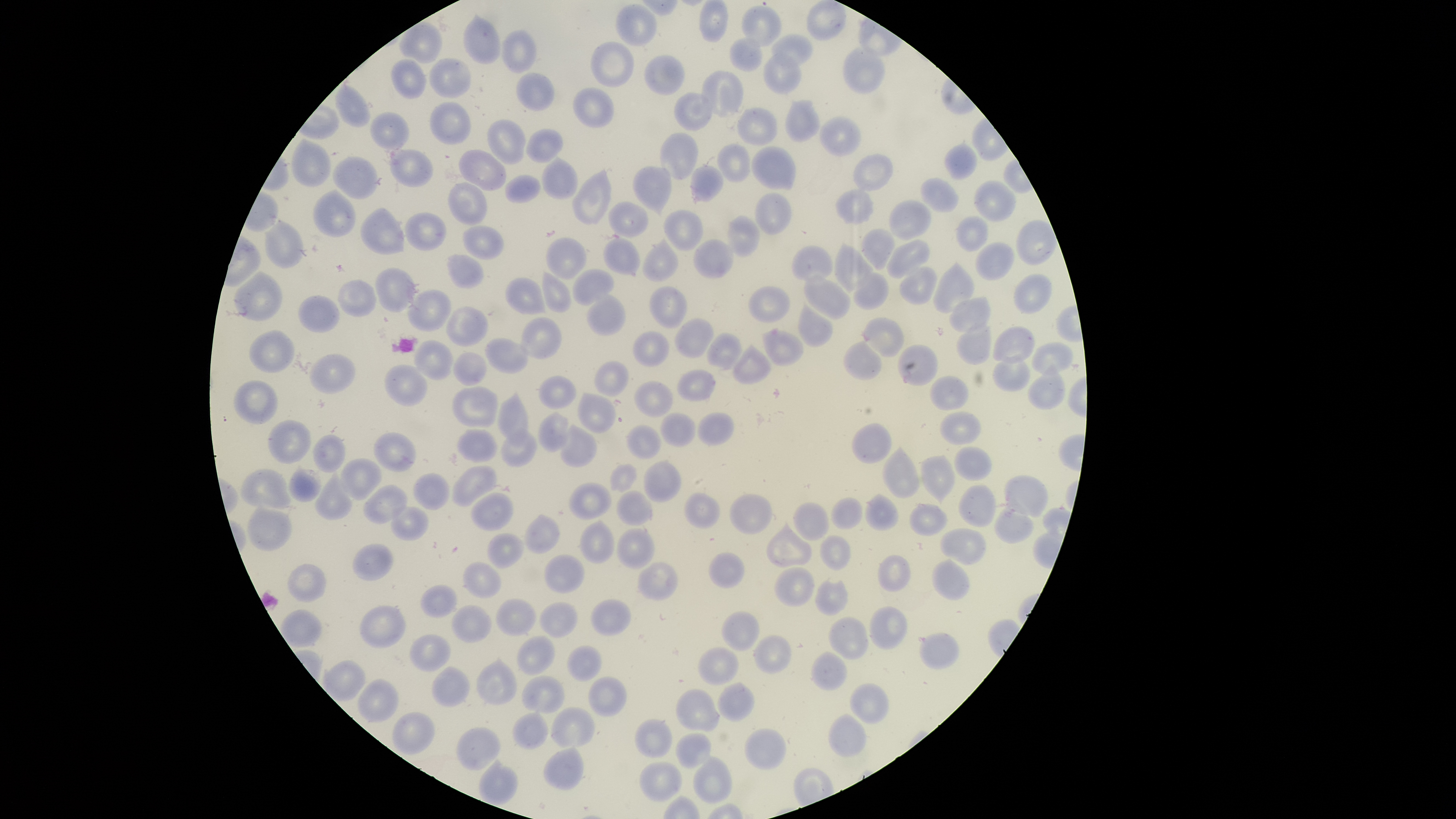
image_size: 1456×819 pixels
presence: no malaria parasites identified
capture: smartphone photograph through the microscope eyepiece
field_of_view: single
preparation: thin blood film
uninfected_red_blood_cells: 'approximate bounding boxes as (left, top, right, bottom) in pixels: (699, 0, 729, 43), (805, 1, 847, 40), (615, 3, 658, 46), (742, 6, 782, 47), (463, 12, 501, 64), (399, 22, 442, 63), (500, 29, 537, 73), (772, 33, 813, 67), (729, 37, 761, 71), (590, 41, 635, 87), (842, 47, 886, 94), (763, 53, 801, 95), (644, 55, 685, 96), (391, 58, 427, 99), (429, 59, 471, 99), (515, 71, 555, 112), (702, 71, 743, 116), (333, 85, 370, 127), (572, 87, 614, 128), (674, 92, 712, 131), (784, 99, 821, 144), (430, 101, 472, 144), (737, 106, 778, 146), (370, 112, 409, 148), (819, 116, 861, 157), (487, 119, 527, 164), (524, 127, 564, 163), (660, 133, 698, 179), (292, 138, 330, 188), (944, 142, 978, 181), (716, 144, 751, 184), (752, 146, 796, 191), (390, 149, 432, 187), (457, 149, 506, 192), (853, 153, 893, 192), (542, 155, 578, 199), (332, 156, 378, 199), (690, 164, 724, 203), (633, 166, 672, 217), (573, 168, 611, 226), (504, 174, 540, 203), (920, 177, 958, 212), (973, 181, 1016, 223), (449, 182, 489, 226), (835, 188, 875, 225), (313, 189, 356, 237), (756, 192, 792, 236), (888, 199, 932, 242), (609, 201, 647, 237), (360, 207, 405, 255), (663, 210, 702, 250), (405, 212, 447, 250), (727, 214, 759, 257), (957, 215, 989, 252), (263, 218, 304, 268), (1015, 220, 1057, 265), (461, 225, 504, 259), (860, 227, 896, 271), (545, 237, 587, 279), (643, 237, 679, 282), (603, 238, 640, 275), (693, 239, 733, 279), (886, 239, 930, 279), (835, 241, 873, 293), (974, 242, 1014, 281), (792, 246, 832, 282), (446, 254, 483, 289), (933, 262, 974, 314), (899, 265, 937, 305), (375, 267, 419, 312), (572, 269, 614, 306), (235, 270, 283, 321), (542, 271, 572, 313), (804, 271, 852, 319), (853, 272, 887, 310), (1013, 274, 1051, 314), (506, 277, 546, 315), (338, 279, 375, 316), (649, 285, 687, 329), (748, 285, 790, 322), (406, 289, 453, 332), (587, 294, 626, 336), (298, 295, 338, 333), (949, 296, 990, 333), (797, 302, 833, 348), (445, 306, 488, 346), (519, 317, 562, 359), (673, 317, 713, 358), (863, 317, 904, 358), (957, 321, 989, 363), (993, 325, 1034, 365), (762, 329, 804, 367), (249, 330, 296, 372), (633, 331, 670, 367), (706, 332, 743, 372), (485, 338, 530, 373), (842, 339, 882, 380), (413, 340, 454, 381), (732, 342, 771, 384), (1032, 343, 1073, 375), (896, 344, 939, 385), (452, 352, 487, 386), (310, 353, 355, 394), (992, 357, 1031, 391), (593, 361, 628, 397), (1028, 363, 1064, 410), (384, 364, 428, 407), (676, 369, 715, 401), (537, 376, 577, 409), (930, 376, 969, 409), (234, 380, 277, 425), (634, 380, 673, 417), (453, 387, 498, 427), (498, 391, 528, 448), (577, 392, 616, 434), (539, 411, 568, 452), (659, 412, 697, 448), (697, 412, 734, 446), (940, 412, 982, 444), (268, 420, 311, 463), (561, 423, 598, 468), (851, 423, 891, 464), (625, 425, 661, 459), (501, 427, 537, 466), (456, 428, 498, 462), (373, 432, 417, 472), (311, 434, 345, 472), (882, 445, 920, 499), (953, 446, 992, 481), (921, 454, 956, 506), (340, 459, 381, 500), (643, 460, 681, 502), (610, 463, 637, 493), (287, 464, 321, 502), (451, 466, 497, 507), (241, 469, 291, 509), (315, 469, 355, 521), (413, 473, 449, 511), (1004, 474, 1049, 517), (568, 482, 612, 521), (958, 484, 997, 527), (363, 485, 407, 523), (616, 490, 653, 526), (469, 492, 513, 530), (683, 492, 720, 529), (729, 493, 772, 533), (865, 493, 899, 531), (830, 497, 863, 529), (793, 501, 829, 541), (994, 501, 1033, 543), (909, 502, 948, 536), (247, 505, 292, 551), (390, 506, 429, 541), (523, 513, 561, 554), (580, 519, 614, 564), (765, 521, 812, 568), (615, 527, 656, 569), (940, 528, 988, 566), (487, 533, 524, 569), (819, 534, 851, 572), (352, 543, 393, 581), (708, 552, 744, 588), (544, 554, 585, 594), (877, 555, 911, 592), (931, 558, 970, 600), (463, 562, 501, 599), (637, 562, 679, 600), (287, 563, 326, 602), (774, 567, 814, 607), (815, 579, 848, 617), (420, 585, 457, 618), (495, 599, 537, 636), (590, 599, 633, 636), (539, 602, 578, 639), (450, 604, 492, 643), (358, 605, 406, 649), (868, 606, 908, 650), (280, 609, 321, 647), (722, 611, 760, 651), (827, 616, 869, 661), (920, 632, 959, 669), (409, 634, 451, 672), (753, 634, 791, 675), (516, 635, 556, 676), (567, 645, 602, 682), (697, 647, 738, 685), (811, 651, 847, 691), (475, 656, 518, 705), (321, 659, 365, 700), (431, 666, 470, 707), (521, 675, 565, 714), (588, 676, 627, 717), (356, 678, 399, 723), (717, 681, 754, 721), (849, 683, 889, 724), (675, 689, 720, 731), (550, 706, 596, 748), (512, 711, 548, 750), (392, 712, 435, 755), (828, 713, 867, 758), (634, 719, 673, 758), (456, 727, 500, 771), (744, 728, 786, 770), (675, 732, 712, 769), (543, 746, 584, 790), (694, 755, 732, 803), (478, 759, 518, 806), (639, 761, 682, 802)'
visible_region: circular
stain: Giemsa